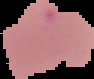

Summary:
  - Image type: cell region segmented out of the field of view; surrounding area masked to black
  - Preparation: thin blood film
  - Result: no malaria parasites detected
  - Image size: 94×79 pixels